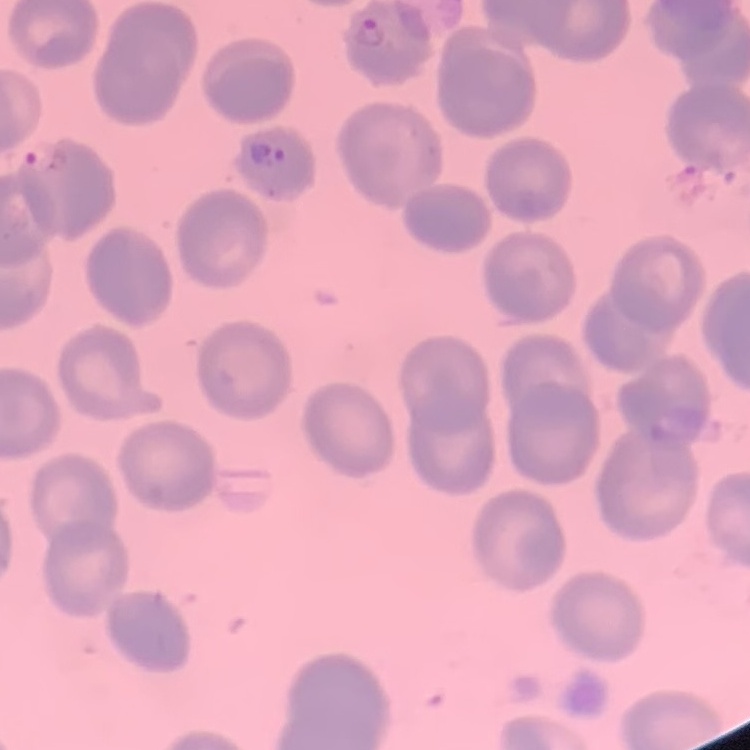
Summary:
  - Red blood cell morphology: no rouleaux formation
  - Stain: Field's or Giemsa
  - Preparation: thin blood film
  - Image type: square crop of a larger photomicrograph